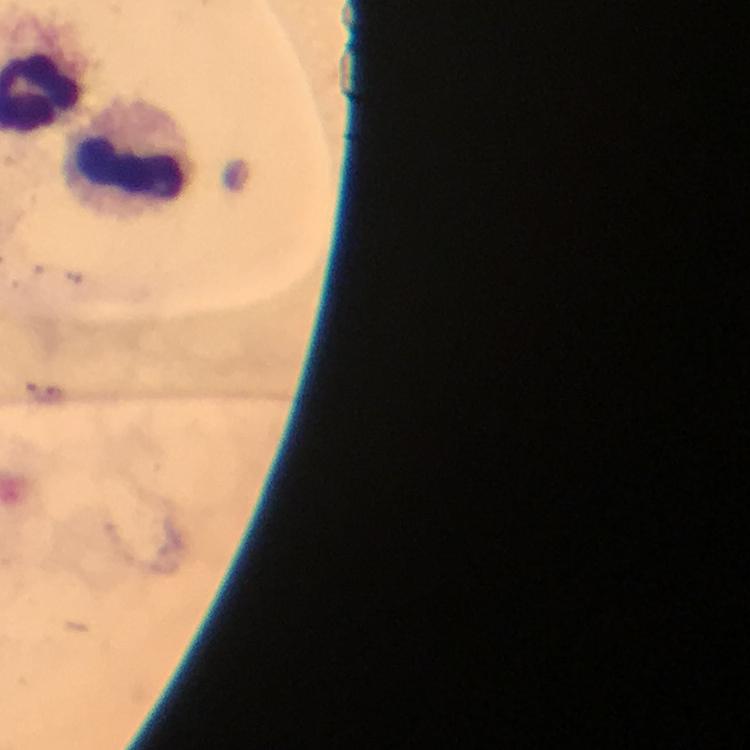
Approximate centers as (x, y) in pixels. Leukocyte locations: (135, 151). Image is 750×750 pixels. Giemsa stain. Photographed with a smartphone mounted on the microscope. At 100x magnification. From a malaria diagnostic workup. Thick smear. Plasmodium parasites: none seen. Immersion oil applied. A crop from one field of view.